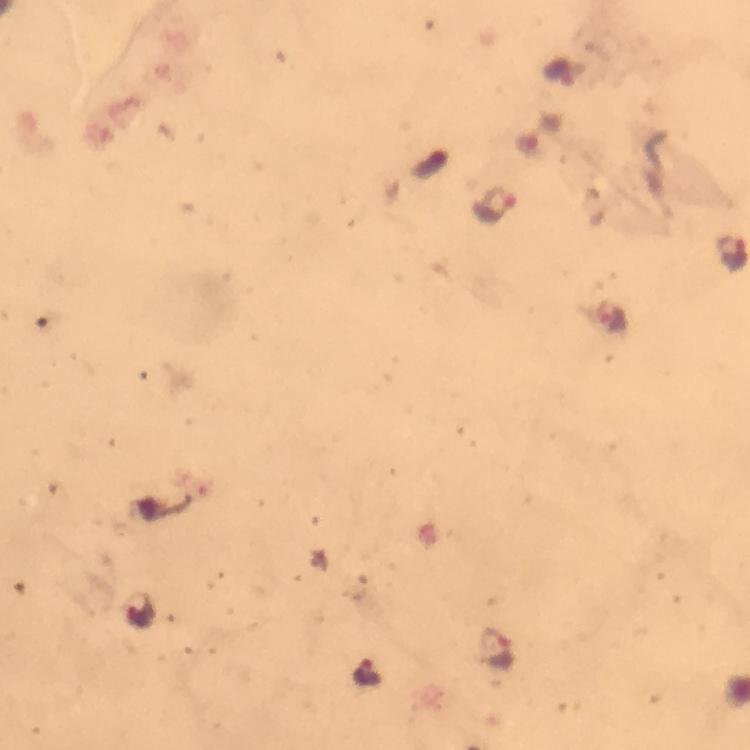
malaria parasite locations = approximate centers as (x, y) in pixels: (558, 75), (495, 204), (612, 319), (140, 612), (497, 650), (368, 673)
context = from a diagnostic examination for malaria
cropped from = one field of view
stain = Giemsa
immersion oil = used
preparation = thick blood smear
capture = smartphone camera through the microscope
image size = 750×750 pixels
magnification = 100x